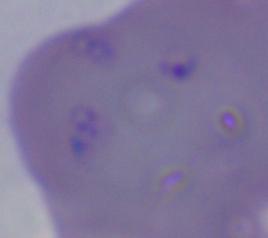
identification = Babesia
modality = micrograph
magnification = 1000x